Report the malaria status of this cell.
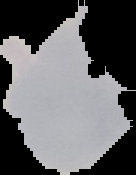
Uninfected.

image type = segmented cell region with the area outside set to black
image size = 136×175 pixels
preparation = thin blood smear